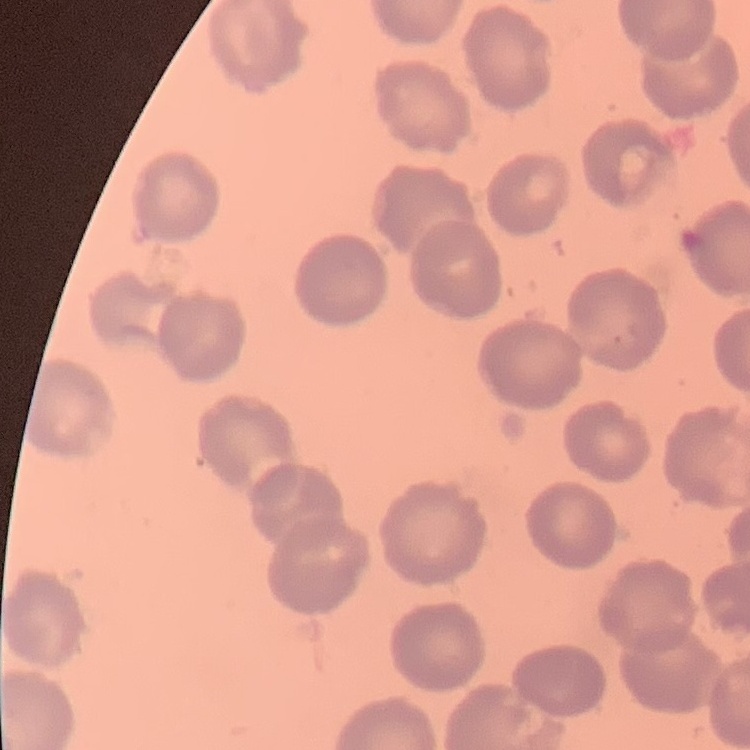
The red blood cells exhibit no rouleaux formation. One tile cut from a larger photomicrograph. Thin peripheral smear. Field's or Giemsa stain.